Assess this cell for malaria.
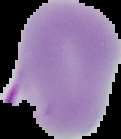

It is parasitized.

{
  "image_size": "121×139 pixels",
  "image_type": "segmented cell region on a black background",
  "preparation": "thin blood film"
}